State the preparation type.
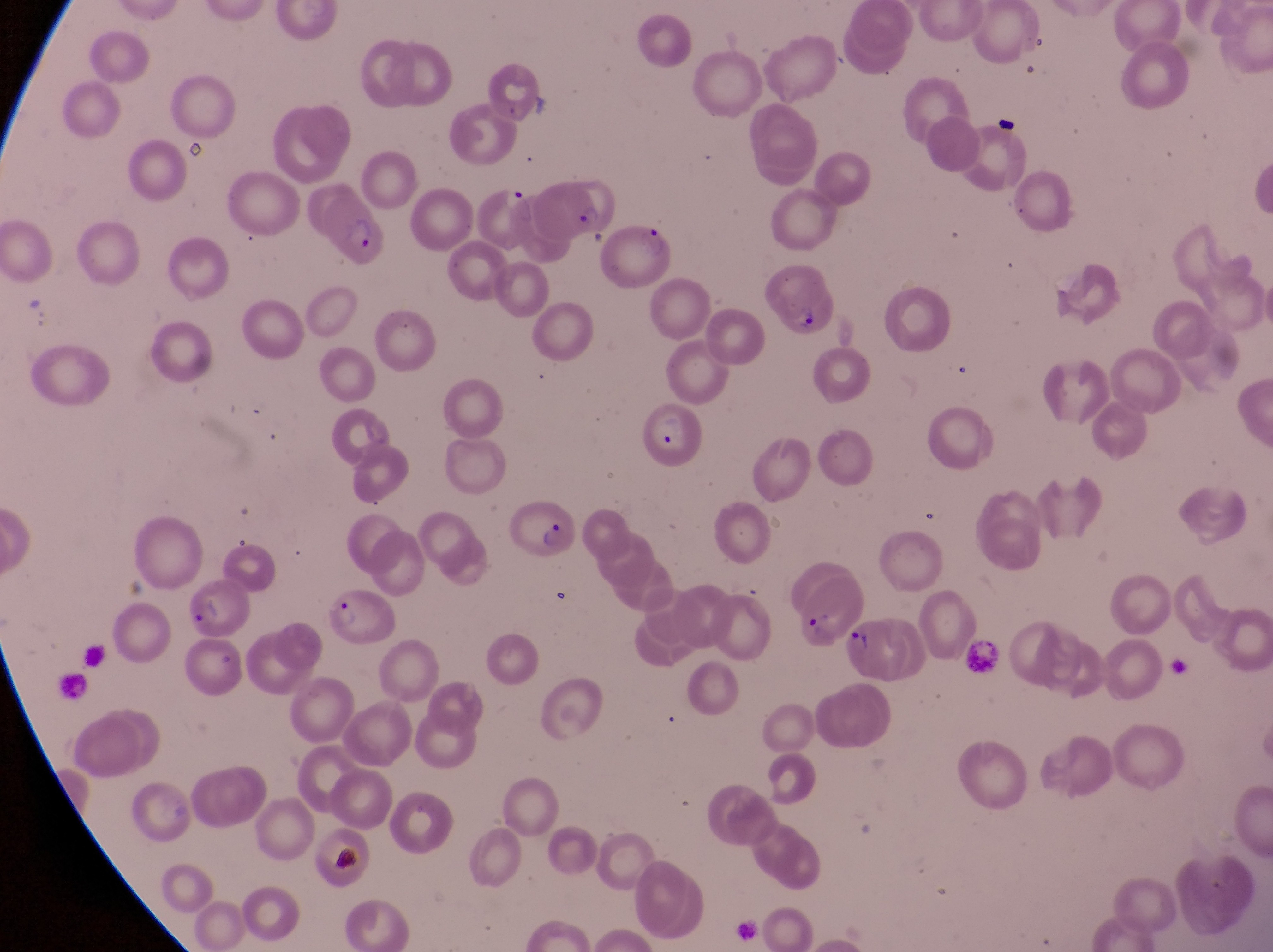
This is a thin smear.

Approximate bounding boxes as {left, top, right, bottom} in pixels. Parasitised red blood cell locations: {534, 174, 609, 234}, {467, 178, 536, 253}, {319, 185, 393, 265}, {601, 220, 679, 292}, {766, 268, 845, 349}, {642, 400, 705, 470}, {507, 497, 582, 569}, {787, 565, 857, 652}, {177, 574, 254, 637}, {329, 587, 401, 650}, {839, 614, 911, 684}, {187, 639, 256, 706}. Leukocyte locations: {965, 634, 1004, 681}. Captured by a smartphone held over the eyepiece of an Olympus CX-23 microscope. Magnification of 1000x. Collected in Uganda. Image is 1273×952 pixels. Single field of view.